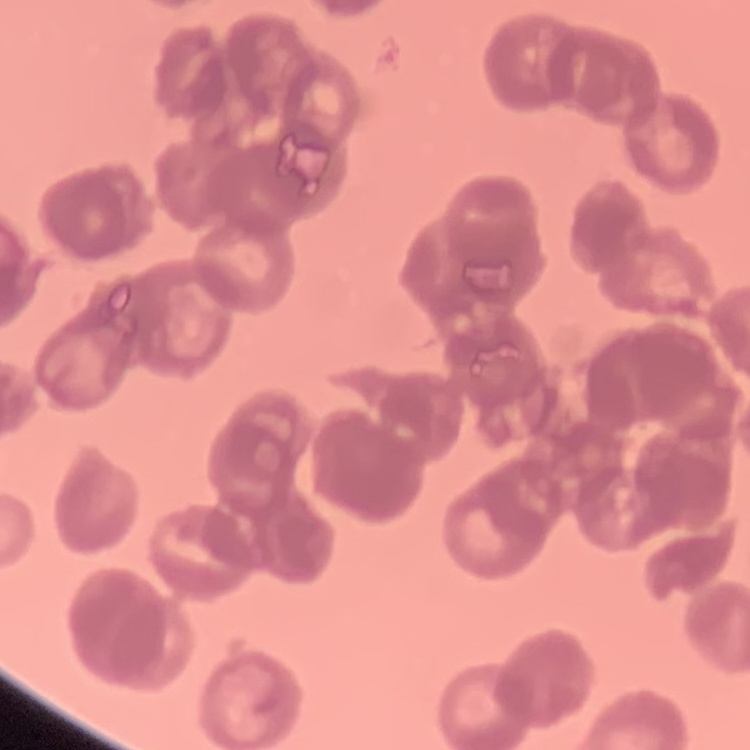
The erythrocytes exhibit rouleaux formation. Stained with either Field's or Giemsa. One tile cut from a larger photomicrograph. Thin blood film.